Assess this cell for malaria.
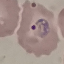
Parasitized.

preparation: thin blood smear
image_type: cell patch, automatically extracted from a larger field of view and resized to 64 × 64 pixels
capture: smartphone camera at the microscope eyepiece
stain: Giemsa